Describe the morphology of the red blood cells.
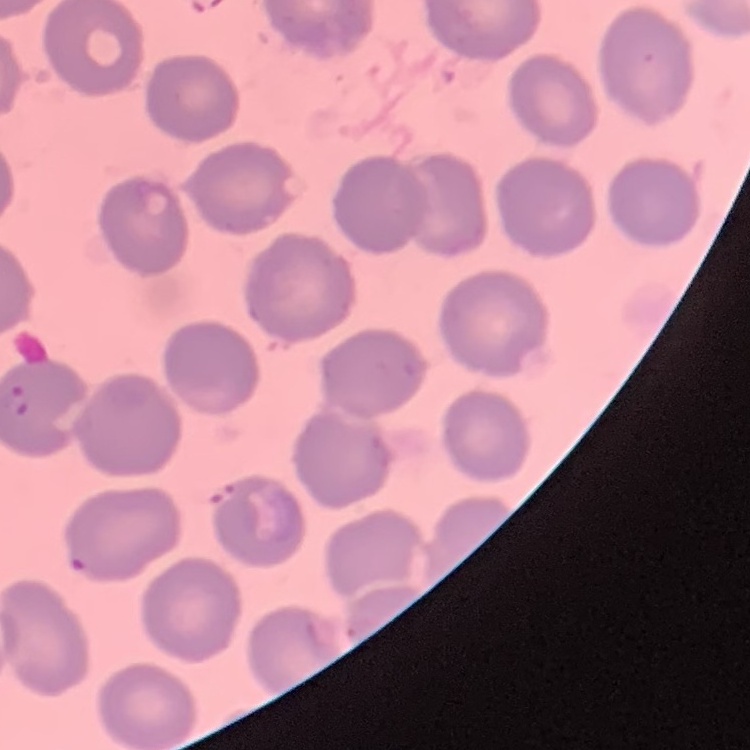

They show no rouleaux formation.

Summary:
  - Image type: one tile cut from a larger photomicrograph
  - Stain: Field's or Giemsa
  - Preparation: thin peripheral smear